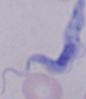
magnification: 1000x
modality: photomicrograph
identification: trypanosome